Name the parasite shown.
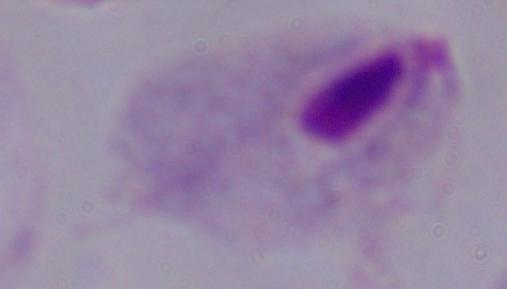

A trichomonad.

Summary:
  - Magnification: 1000x
  - Modality: micrograph